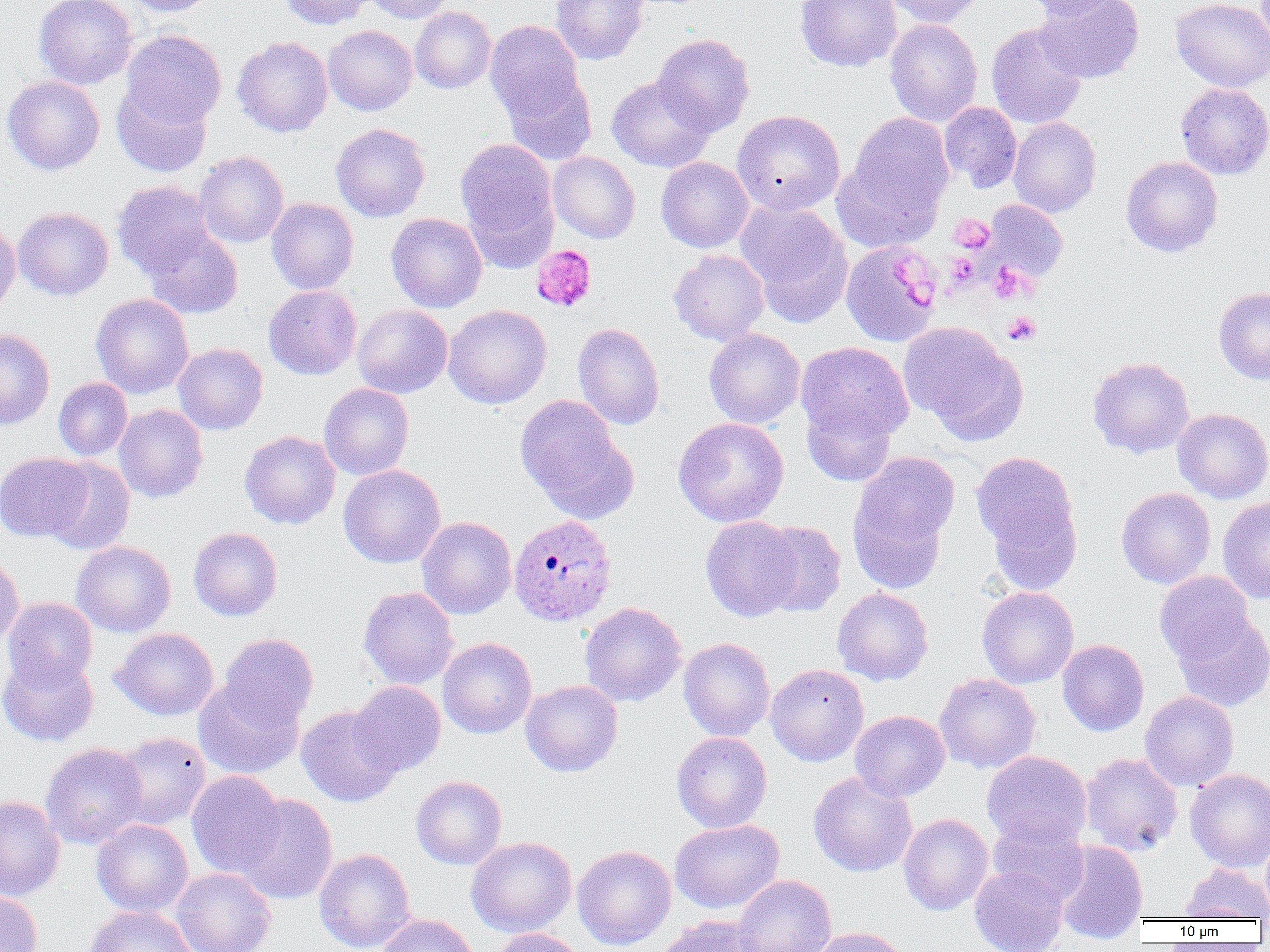

{
  "slide_level_diagnosis": "Plasmodium ovale",
  "image_size": "1270×952 pixels",
  "plasmodium_ovale_infected_red_blood_cell_locations": "approximate bounding boxes as named x1/y1/x2/y2 corners in pixels: (x1=509, y1=513, x2=617, y2=626)",
  "magnification": "1000x",
  "uninfected_red_blood_cell_locations": "approximate bounding boxes as named x1/y1/x2/y2 corners in pixels: (x1=34, y1=0, x2=137, y2=90), (x1=120, y1=0, x2=219, y2=17), (x1=280, y1=0, x2=374, y2=29), (x1=362, y1=0, x2=453, y2=24), (x1=550, y1=0, x2=649, y2=65), (x1=795, y1=0, x2=902, y2=72), (x1=883, y1=0, x2=985, y2=27), (x1=1021, y1=0, x2=1127, y2=20), (x1=1034, y1=0, x2=1144, y2=83), (x1=1170, y1=0, x2=1270, y2=92), (x1=410, y1=7, x2=496, y2=94), (x1=885, y1=18, x2=982, y2=127), (x1=484, y1=20, x2=584, y2=123), (x1=986, y1=22, x2=1088, y2=129), (x1=323, y1=25, x2=418, y2=115), (x1=121, y1=30, x2=226, y2=129), (x1=652, y1=33, x2=754, y2=137), (x1=232, y1=35, x2=333, y2=138), (x1=502, y1=70, x2=598, y2=166), (x1=2, y1=76, x2=105, y2=175), (x1=607, y1=77, x2=714, y2=172), (x1=112, y1=82, x2=212, y2=176), (x1=1175, y1=82, x2=1270, y2=180), (x1=939, y1=101, x2=1023, y2=193), (x1=732, y1=110, x2=845, y2=215), (x1=846, y1=113, x2=954, y2=227), (x1=1008, y1=117, x2=1102, y2=217), (x1=330, y1=123, x2=430, y2=222), (x1=455, y1=139, x2=557, y2=251), (x1=195, y1=151, x2=288, y2=248), (x1=548, y1=151, x2=640, y2=244), (x1=832, y1=156, x2=944, y2=253), (x1=1121, y1=156, x2=1223, y2=257), (x1=656, y1=157, x2=754, y2=253), (x1=111, y1=181, x2=217, y2=278), (x1=267, y1=198, x2=359, y2=294), (x1=735, y1=200, x2=852, y2=323), (x1=983, y1=200, x2=1068, y2=282), (x1=12, y1=207, x2=114, y2=300), (x1=386, y1=212, x2=487, y2=313), (x1=0, y1=222, x2=21, y2=315), (x1=142, y1=225, x2=244, y2=320), (x1=840, y1=241, x2=942, y2=347), (x1=669, y1=249, x2=770, y2=345), (x1=264, y1=285, x2=361, y2=380), (x1=1214, y1=287, x2=1270, y2=385), (x1=91, y1=293, x2=194, y2=398), (x1=352, y1=305, x2=453, y2=398), (x1=443, y1=305, x2=552, y2=409), (x1=899, y1=322, x2=1025, y2=441), (x1=573, y1=323, x2=665, y2=430), (x1=704, y1=328, x2=805, y2=428), (x1=0, y1=329, x2=55, y2=430), (x1=796, y1=341, x2=914, y2=445), (x1=172, y1=343, x2=268, y2=435), (x1=1088, y1=356, x2=1194, y2=458), (x1=53, y1=378, x2=133, y2=460), (x1=319, y1=383, x2=414, y2=480), (x1=515, y1=395, x2=635, y2=521), (x1=802, y1=399, x2=897, y2=487), (x1=114, y1=404, x2=208, y2=503), (x1=1172, y1=408, x2=1270, y2=504), (x1=672, y1=417, x2=789, y2=527), (x1=239, y1=430, x2=341, y2=529), (x1=971, y1=451, x2=1082, y2=576), (x1=0, y1=452, x2=92, y2=542), (x1=849, y1=452, x2=959, y2=583), (x1=42, y1=456, x2=135, y2=555), (x1=338, y1=464, x2=446, y2=568), (x1=1116, y1=487, x2=1216, y2=589), (x1=1217, y1=496, x2=1270, y2=604), (x1=700, y1=515, x2=803, y2=622), (x1=417, y1=516, x2=516, y2=619), (x1=756, y1=520, x2=846, y2=617), (x1=188, y1=527, x2=283, y2=621), (x1=71, y1=541, x2=176, y2=637), (x1=0, y1=552, x2=24, y2=650), (x1=1154, y1=570, x2=1254, y2=665), (x1=977, y1=586, x2=1078, y2=688), (x1=358, y1=587, x2=459, y2=689), (x1=832, y1=587, x2=933, y2=685), (x1=2, y1=597, x2=98, y2=690), (x1=580, y1=602, x2=686, y2=706), (x1=1171, y1=609, x2=1270, y2=712), (x1=110, y1=628, x2=219, y2=720), (x1=218, y1=633, x2=319, y2=729), (x1=437, y1=637, x2=536, y2=739), (x1=678, y1=638, x2=775, y2=741), (x1=1057, y1=638, x2=1149, y2=736), (x1=0, y1=652, x2=99, y2=747), (x1=766, y1=664, x2=868, y2=766), (x1=934, y1=673, x2=1041, y2=773), (x1=193, y1=678, x2=304, y2=779), (x1=520, y1=680, x2=623, y2=776), (x1=349, y1=681, x2=446, y2=776), (x1=1140, y1=691, x2=1239, y2=792), (x1=296, y1=705, x2=402, y2=807), (x1=850, y1=710, x2=950, y2=802), (x1=112, y1=732, x2=211, y2=830), (x1=671, y1=732, x2=772, y2=832), (x1=40, y1=742, x2=148, y2=849), (x1=981, y1=750, x2=1092, y2=848), (x1=1081, y1=752, x2=1183, y2=856), (x1=1185, y1=768, x2=1270, y2=871), (x1=186, y1=770, x2=286, y2=878), (x1=807, y1=771, x2=918, y2=877), (x1=411, y1=776, x2=507, y2=870), (x1=235, y1=794, x2=338, y2=905), (x1=0, y1=795, x2=65, y2=902), (x1=898, y1=813, x2=993, y2=916), (x1=987, y1=816, x2=1089, y2=907), (x1=91, y1=818, x2=193, y2=917), (x1=670, y1=819, x2=784, y2=914), (x1=1260, y1=835, x2=1270, y2=917), (x1=466, y1=837, x2=576, y2=937), (x1=1053, y1=840, x2=1148, y2=943), (x1=573, y1=845, x2=676, y2=950), (x1=314, y1=848, x2=415, y2=952), (x1=1180, y1=862, x2=1269, y2=920), (x1=970, y1=865, x2=1069, y2=952), (x1=170, y1=867, x2=276, y2=952), (x1=732, y1=874, x2=836, y2=952), (x1=0, y1=891, x2=44, y2=952), (x1=82, y1=905, x2=197, y2=952), (x1=376, y1=913, x2=479, y2=952), (x1=658, y1=916, x2=765, y2=952), (x1=808, y1=926, x2=910, y2=952), (x1=491, y1=928, x2=585, y2=952)",
  "modality": "light microscopy",
  "preparation": "thin blood smear",
  "platelet_locations": "approximate bounding boxes as named x1/y1/x2/y2 corners in pixels: (x1=949, y1=214, x2=994, y2=253), (x1=531, y1=245, x2=597, y2=312), (x1=946, y1=252, x2=979, y2=288), (x1=892, y1=258, x2=925, y2=281), (x1=988, y1=263, x2=1033, y2=303), (x1=910, y1=285, x2=934, y2=311), (x1=1003, y1=312, x2=1041, y2=346)",
  "field_of_view": "single"
}